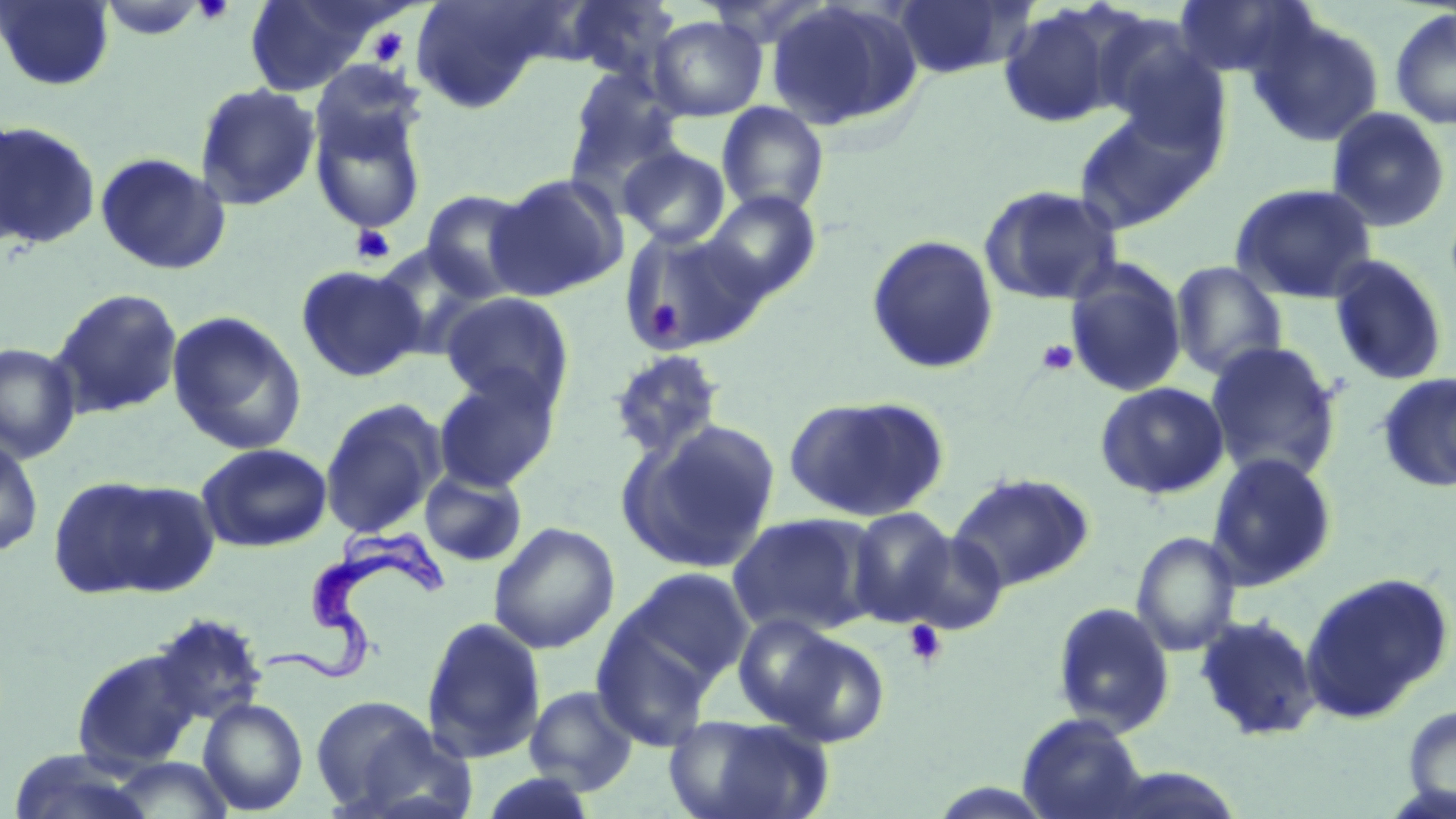
Summary:
  - Coordinate format: approximate bounding boxes as [x1, y1, x2, y2] in pixels
  - Uninfected red blood cell locations: [0, 0, 116, 90], [243, 0, 387, 96], [561, 0, 682, 85], [765, 0, 924, 133], [890, 0, 1032, 79], [1174, 0, 1316, 80], [409, 1, 557, 113], [97, 2, 209, 42], [996, 3, 1127, 129], [1389, 7, 1456, 130], [647, 15, 768, 121], [1248, 15, 1385, 148], [309, 60, 425, 164], [563, 65, 686, 199], [194, 82, 321, 210], [308, 98, 429, 235], [716, 102, 829, 217], [1326, 107, 1452, 233], [1074, 108, 1213, 233], [0, 111, 28, 250], [0, 120, 100, 250], [618, 145, 731, 249], [95, 151, 231, 276], [488, 173, 627, 301], [1230, 182, 1378, 304], [978, 184, 1126, 307], [419, 190, 537, 303], [702, 191, 821, 301], [618, 226, 764, 356], [866, 234, 1000, 375], [371, 244, 497, 360], [1328, 255, 1449, 387], [1064, 259, 1188, 398], [1169, 261, 1288, 381], [295, 264, 426, 381], [49, 287, 184, 419], [440, 292, 574, 410], [167, 311, 306, 456], [1204, 340, 1343, 483], [0, 342, 81, 463], [607, 348, 727, 461], [432, 369, 561, 492], [1377, 372, 1456, 492], [1094, 381, 1230, 500], [783, 395, 948, 522], [319, 398, 446, 540], [620, 419, 780, 573], [0, 434, 44, 559], [196, 443, 332, 553], [1206, 452, 1338, 589], [419, 468, 527, 567], [949, 472, 1095, 592], [48, 474, 216, 601], [847, 507, 957, 625], [726, 513, 878, 636], [488, 521, 620, 654], [898, 530, 1008, 636], [1131, 531, 1240, 656], [613, 568, 754, 694], [1300, 571, 1453, 722], [1051, 602, 1175, 736], [732, 613, 844, 729], [1195, 613, 1322, 742], [421, 616, 547, 764], [591, 621, 719, 751], [772, 631, 891, 747], [70, 647, 204, 772], [525, 685, 640, 795], [307, 694, 464, 818], [197, 697, 308, 814], [1402, 704, 1456, 813], [665, 713, 833, 819], [1016, 714, 1149, 819], [7, 748, 156, 819], [105, 756, 239, 818], [478, 770, 601, 818]
  - Platelet locations: [194, 0, 234, 24], [368, 27, 409, 66], [350, 224, 396, 265], [642, 296, 685, 337], [1036, 339, 1078, 376], [904, 620, 947, 667]
  - Trypanosoma brucei locations: [262, 517, 454, 684]
  - Slide-level diagnosis: Trypanosoma brucei
  - Field of view: single
  - Magnification: 1000x
  - Image size: 1456×819 pixels
  - Preparation: thin blood smear
  - Modality: optical microscopy
  - Stain: May-Grünwald-Giemsa